State the preparation type.
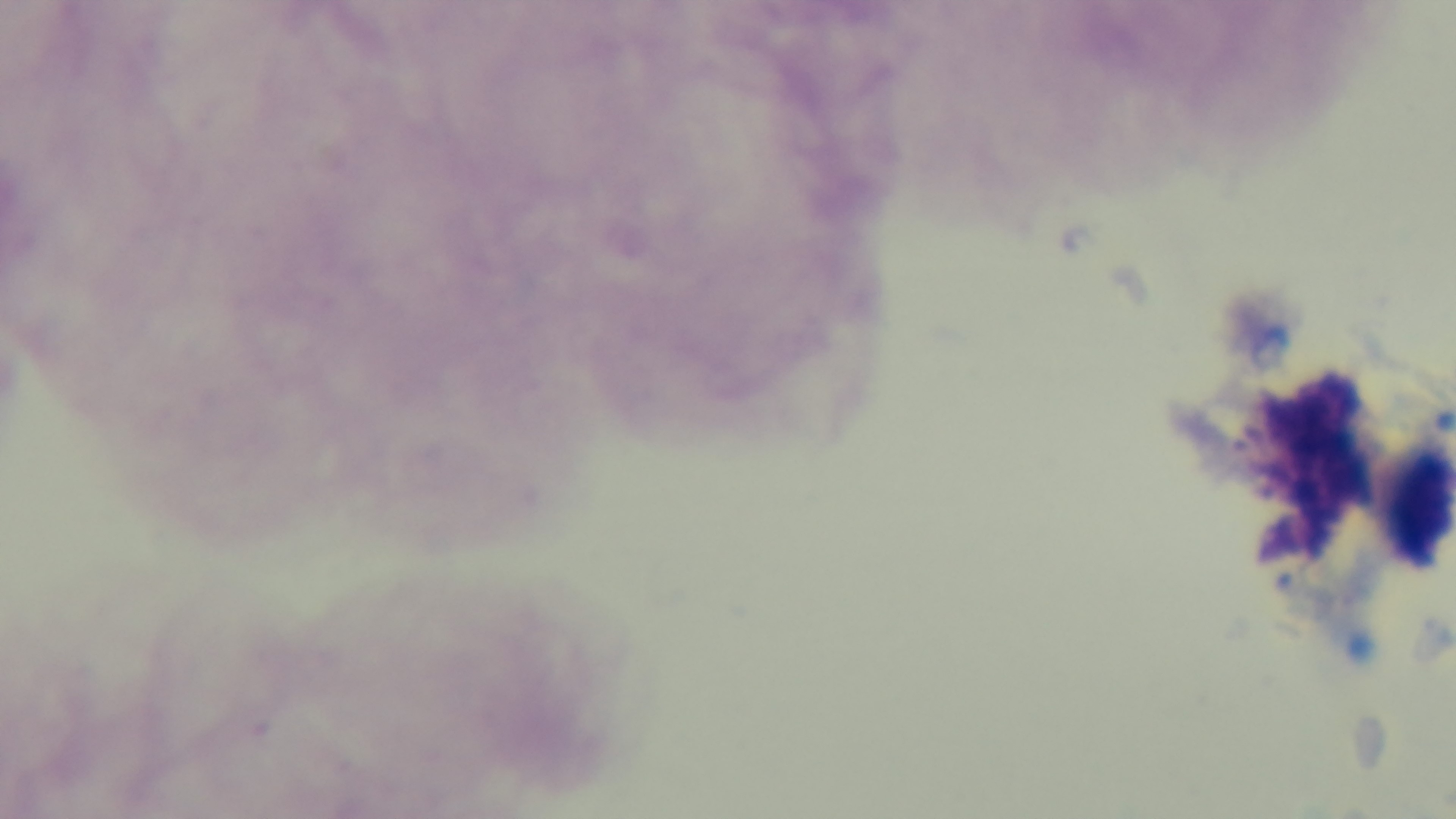

Thick.

Mounted 4K digital camera. Light microscopy. Giemsa-stained. Single field of view. Malaria status: uninfected. Oil-immersion objective, 100x.